Classify this cell by malaria status.
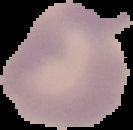

It is uninfected.

Summary:
  - Preparation: thin blood film
  - Image size: 133×130 pixels
  - Image type: segmented cell region with the area outside set to black